Locate every Plasmodium parasite.
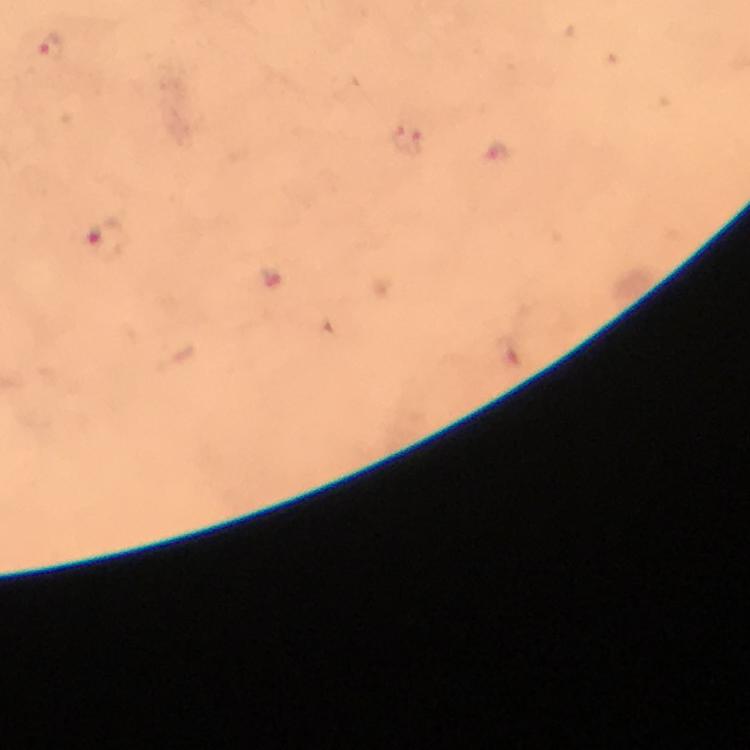

Approximate centers as {x, y} in pixels.
Plasmodium parasites: {49, 48}, {408, 142}, {106, 239}.

immersion oil = applied
capture = smartphone camera through the microscope
stain = Giemsa
cropped from = a single field of view
magnification = 100x
context = from a diagnostic examination for malaria
image size = 750×750 pixels
preparation = thick blood smear